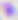

identification = Toxoplasma gondii
magnification = 400x
modality = micrograph